Assess this cell for malaria.
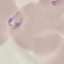

Parasitized.

image type = automatically extracted cell patch, resized to 64 × 64 pixels
capture = smartphone camera at the microscope eyepiece
stain = Giemsa
preparation = thin smear